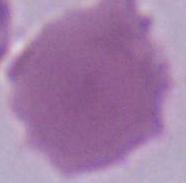

An erythrocyte is shown. 1000x magnification. Photomicrograph.